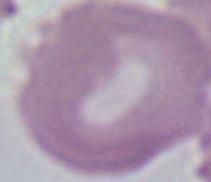

Summary:
  - Magnification: 1000x
  - Modality: photomicrograph
  - Identification: erythrocyte